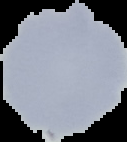 Cell region segmented out of the field of view; the surrounding area is masked to black. From a thin blood film. Result: negative for malaria parasites. Image is 127×142 pixels.